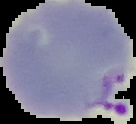

image size = 136×124 pixels
preparation = thin blood film
image type = segmented cell region on a black background
result = Plasmodium parasites identified